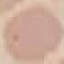

Result: no malaria parasites seen. Giemsa stain. Photographed with a smartphone camera at the microscope eyepiece. Thin smear of blood. Automatically extracted cell patch, resized to 64 × 64 pixels.